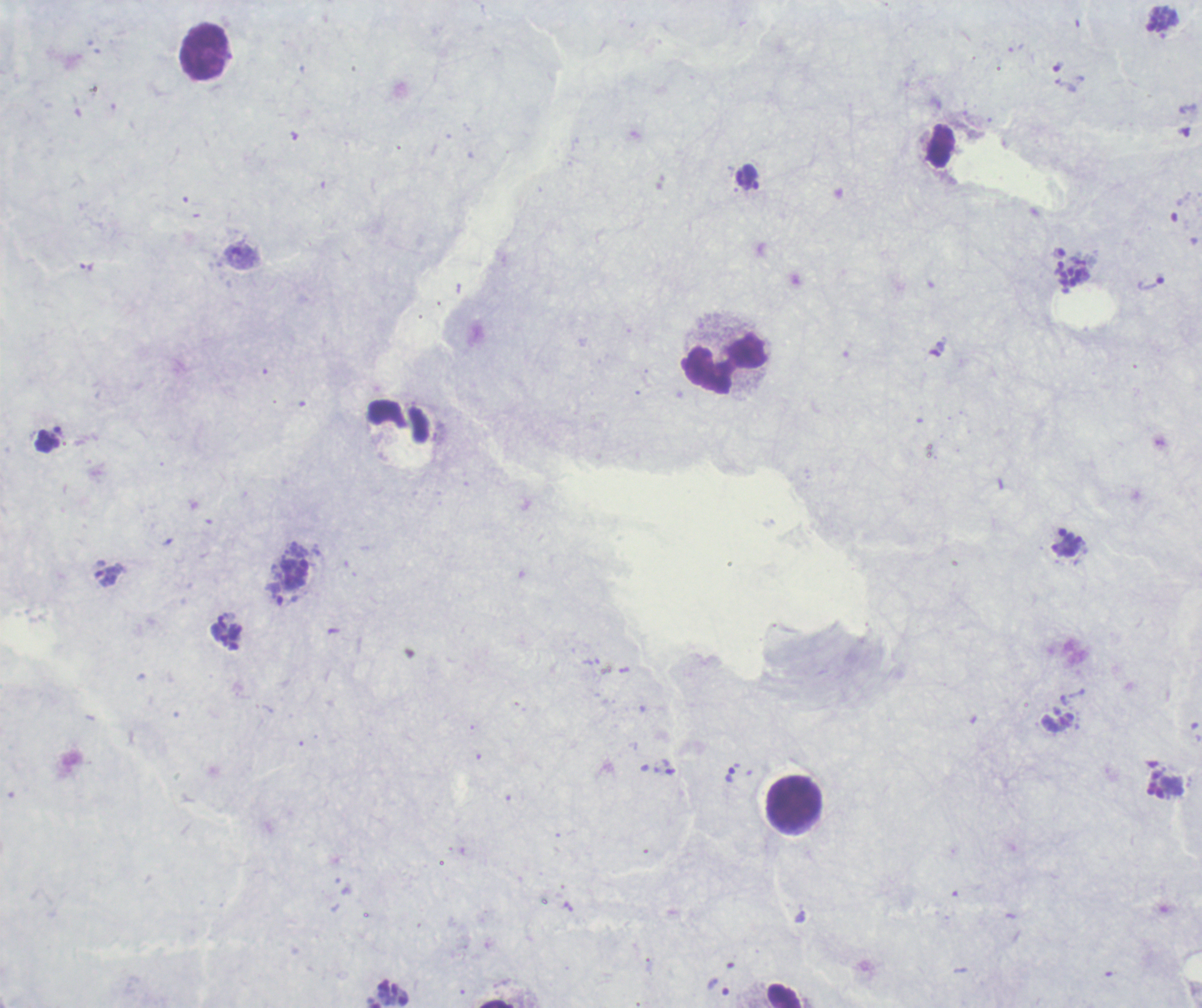

life_cycle_stages_observed: trophozoite, schizont
stain: Romanowsky
background_quality: poor
result: malaria parasites identified
magnification: 100x
context: previously used in a real diagnosis
field_of_view: one from this slide
schizont_locations: 'approximate object centers, in pixels from the top-left corner: (x=1163, y=20), (x=1073, y=270)'
preparation: thick blood smear
trophozoite_locations: 'approximate object centers, in pixels from the top-left corner: (x=1151, y=283), (x=276, y=593), (x=730, y=774), (x=719, y=988)'
leukocyte_locations: 'approximate object centers, in pixels from the top-left corner: (x=204, y=50), (x=725, y=365), (x=794, y=804), (x=785, y=995)'
image_size: 1202×1008 pixels